Describe the morphology of the red blood cells.
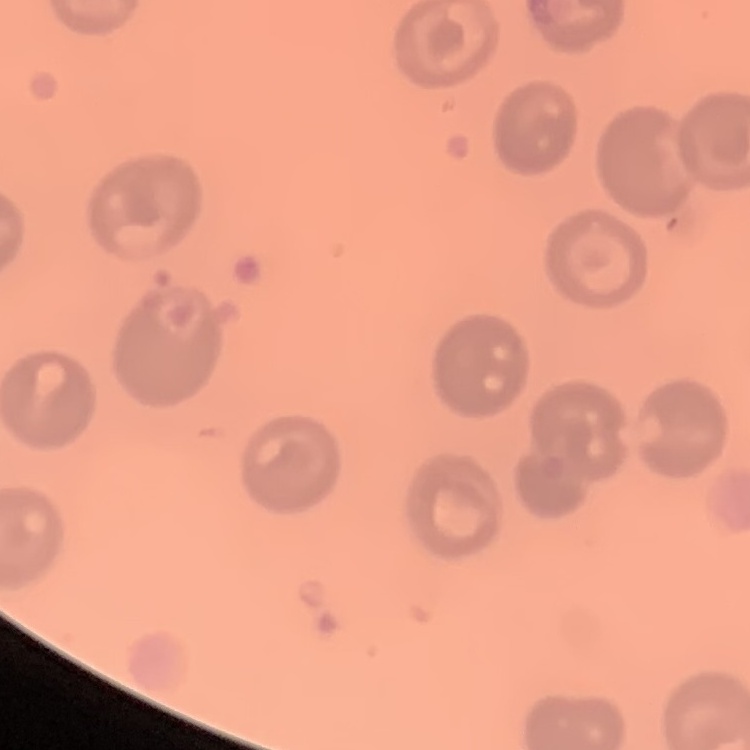

No rouleaux formation.

image_type: one tile cut from a larger photomicrograph
stain: Field's or Giemsa
preparation: thin peripheral smear